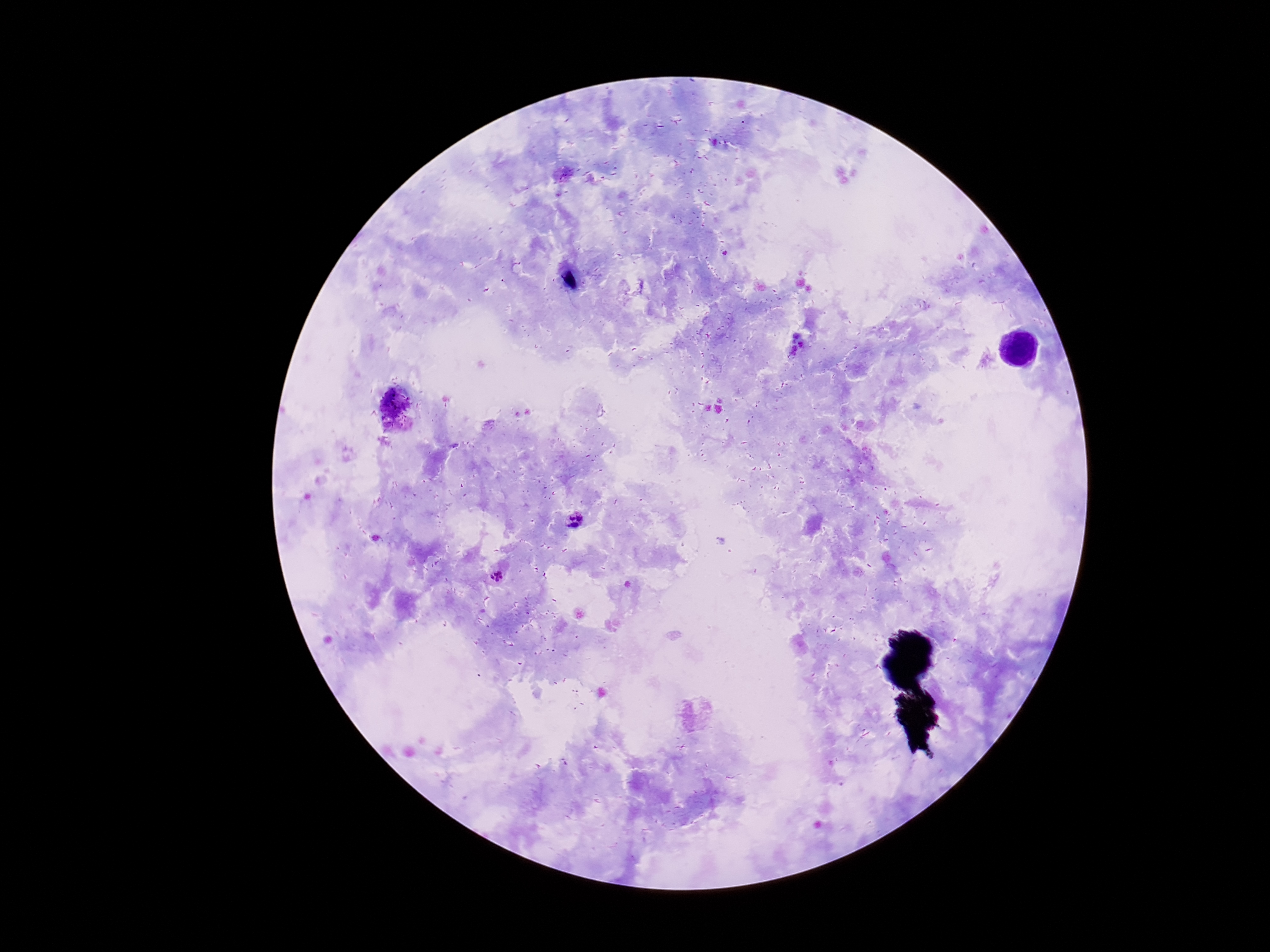

Plasmodium parasite locations = approximate object centers, in pixels from the top-left corner: (x=574, y=521), (x=499, y=577)
magnification = 100x
field of view = one from this slide
preparation = thick blood film
patient malaria status = infected
stain = Giemsa
image size = 1270×952 pixels
capture = smartphone camera through the microscope eyepiece